Assess this cell for malaria.
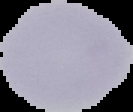
Uninfected.

preparation = thin blood film
image type = segmented cell region on a black background
image size = 133×112 pixels